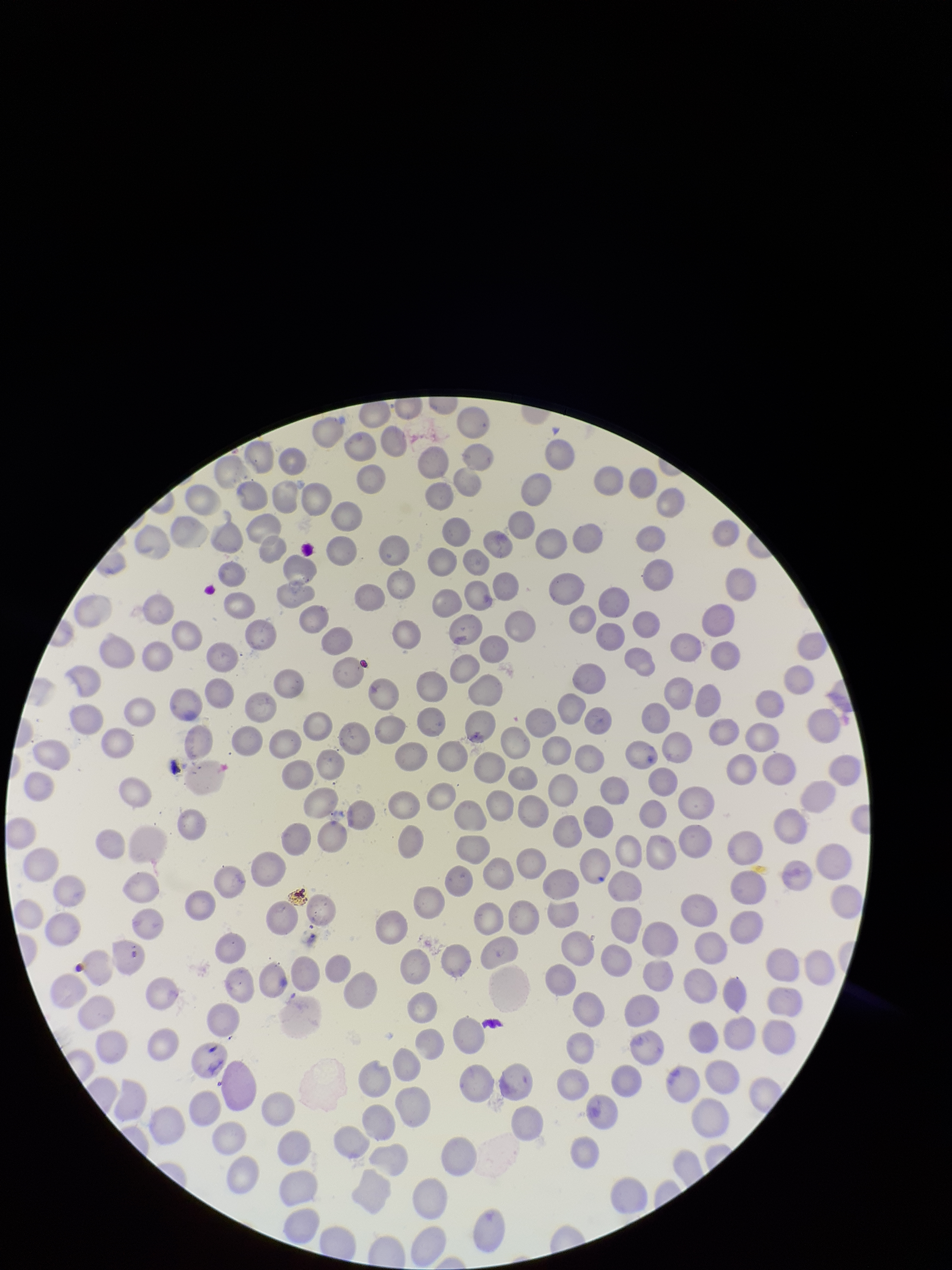
Summary:
  - Preparation: thin blood smear
  - Capture: smartphone photograph through the microscope eyepiece
  - Species reported for this patient: Plasmodium falciparum
  - Field of view: one from this slide
  - Parasitized red blood cells: none identified
  - Red blood cell count: 247
  - Patient malaria status: infected
  - Stain: Giemsa
  - Image size: 952×1270 pixels
  - Parasitized red blood cell count: 0